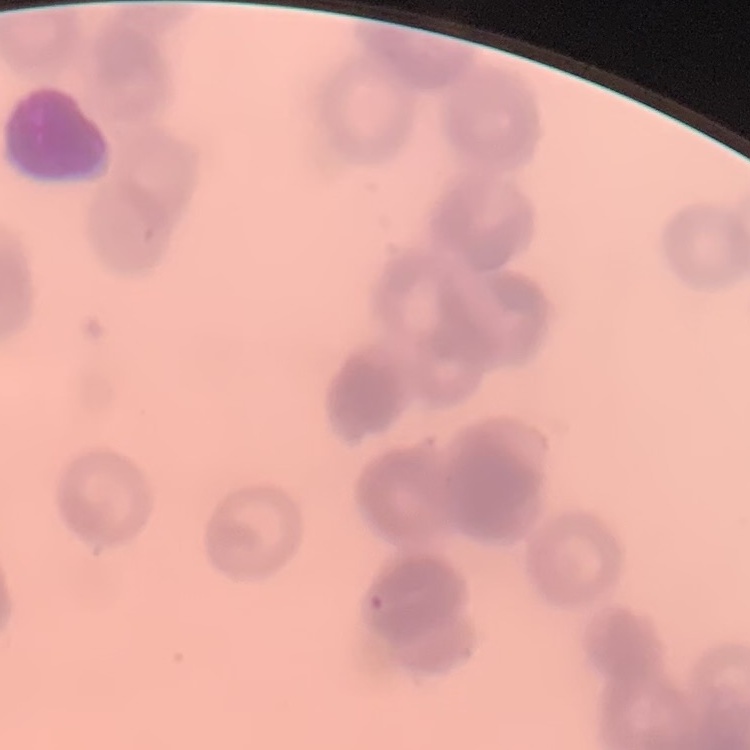
{
  "erythrocyte_morphology": "rouleaux formation",
  "stain": "Field's or Giemsa",
  "image_type": "one tile cut from a larger photomicrograph",
  "preparation": "thin peripheral smear"
}